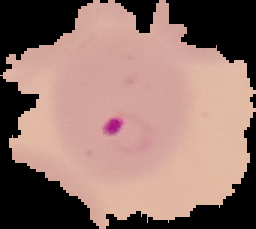
Segmented cell region on a black background. Result: malaria parasites identified. From a thin blood film. Image is 256×229 pixels.